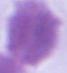
{
  "magnification": "1000x",
  "modality": "micrograph",
  "identification": "erythrocyte"
}